Identify the parasite.
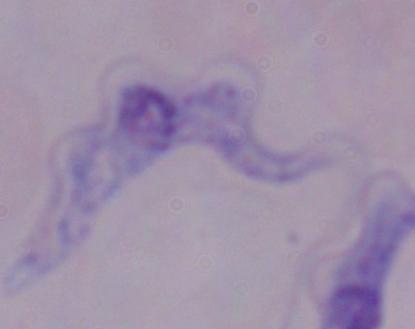
A trypanosome.

Summary:
  - Magnification: 1000x
  - Modality: micrograph